Identify the parasite.
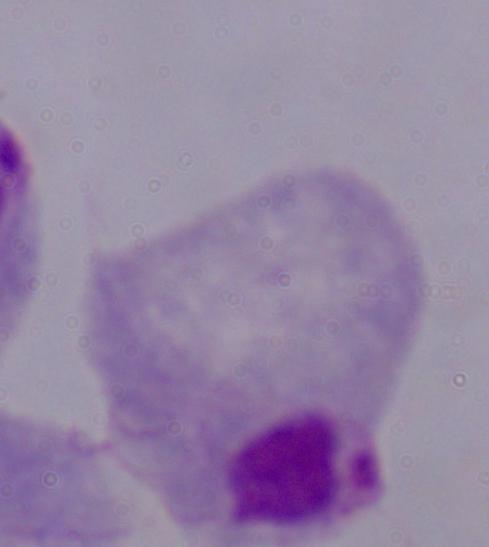
This is a trichomonad.

Captured at 1000x magnification. Photomicrograph.